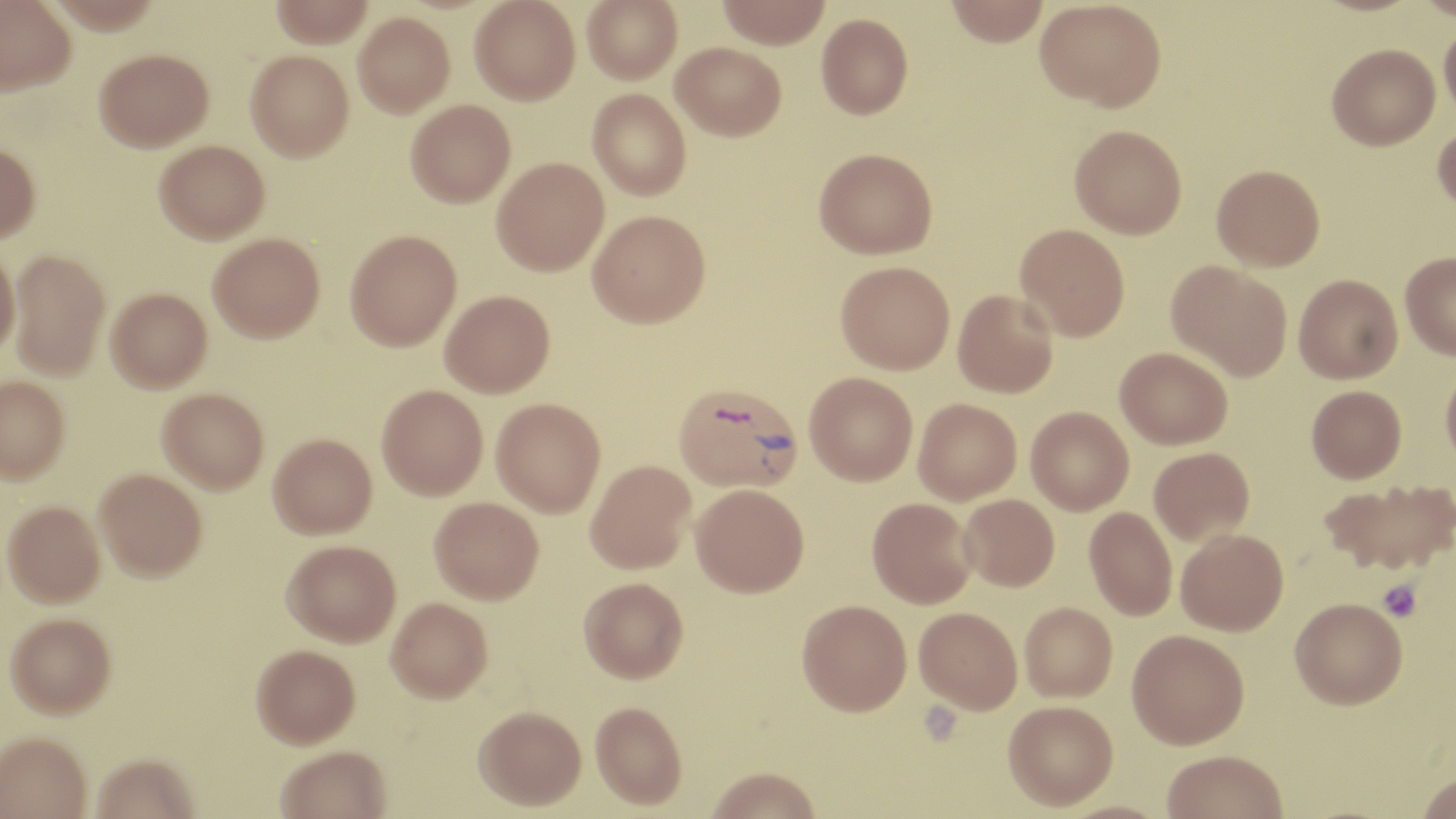
Summary:
  - Coordinate format: approximate bounding boxes as (x1, y1, x2, y2) in pixels
  - Plasmodium vivax-infected red blood cell locations: (674, 381, 803, 493)
  - Platelet locations: (1378, 580, 1422, 622)
  - Uninfected red blood cell locations: (0, 0, 77, 95), (267, 0, 375, 46), (470, 0, 580, 105), (582, 0, 682, 83), (717, 0, 831, 49), (945, 0, 1050, 46), (1035, 0, 1166, 112), (353, 11, 455, 117), (816, 13, 913, 118), (1439, 16, 1456, 120), (671, 42, 786, 140), (1327, 43, 1440, 150), (93, 48, 213, 152), (245, 50, 354, 162), (588, 88, 691, 200), (405, 100, 515, 207), (1432, 122, 1456, 215), (1069, 124, 1187, 238), (154, 139, 269, 243), (0, 143, 41, 244), (814, 147, 937, 259), (491, 157, 609, 275), (1211, 163, 1325, 270), (588, 210, 711, 327), (1015, 223, 1130, 341), (345, 229, 462, 351), (207, 232, 324, 342), (0, 247, 19, 356), (8, 248, 110, 379), (1399, 252, 1456, 359), (835, 260, 955, 374), (1166, 260, 1293, 380), (1293, 273, 1403, 383), (106, 287, 212, 392), (953, 289, 1059, 398), (440, 290, 555, 397), (1115, 346, 1232, 449), (1440, 361, 1456, 470), (805, 372, 918, 485), (0, 375, 71, 483), (376, 384, 488, 499), (1306, 385, 1407, 482), (157, 387, 269, 493), (491, 398, 606, 517), (913, 398, 1022, 504), (1026, 406, 1134, 515), (267, 433, 377, 539), (1149, 447, 1254, 546), (585, 459, 696, 574), (94, 467, 207, 581), (1319, 478, 1456, 576), (691, 483, 809, 596), (959, 494, 1059, 591), (429, 496, 544, 603), (867, 497, 977, 608), (3, 500, 105, 607), (1084, 507, 1177, 620), (1176, 528, 1289, 635), (281, 539, 401, 646), (579, 577, 688, 683), (386, 597, 493, 703), (1290, 597, 1407, 708), (797, 599, 912, 716), (1019, 602, 1118, 701), (914, 606, 1023, 713), (5, 611, 117, 718), (1127, 629, 1249, 749), (251, 643, 360, 748), (590, 701, 687, 810), (1002, 701, 1118, 810), (474, 706, 586, 811), (0, 731, 92, 819), (275, 746, 392, 819), (1161, 750, 1289, 819), (90, 752, 201, 819), (705, 768, 822, 819), (1416, 771, 1456, 819)
  - Slide-level diagnosis: Plasmodium vivax
  - Modality: light microscopy
  - Preparation: thin blood smear
  - Image size: 1456×819 pixels
  - Stain: May-Grünwald-Giemsa
  - Field of view: one of a larger specimen
  - Magnification: 1000x